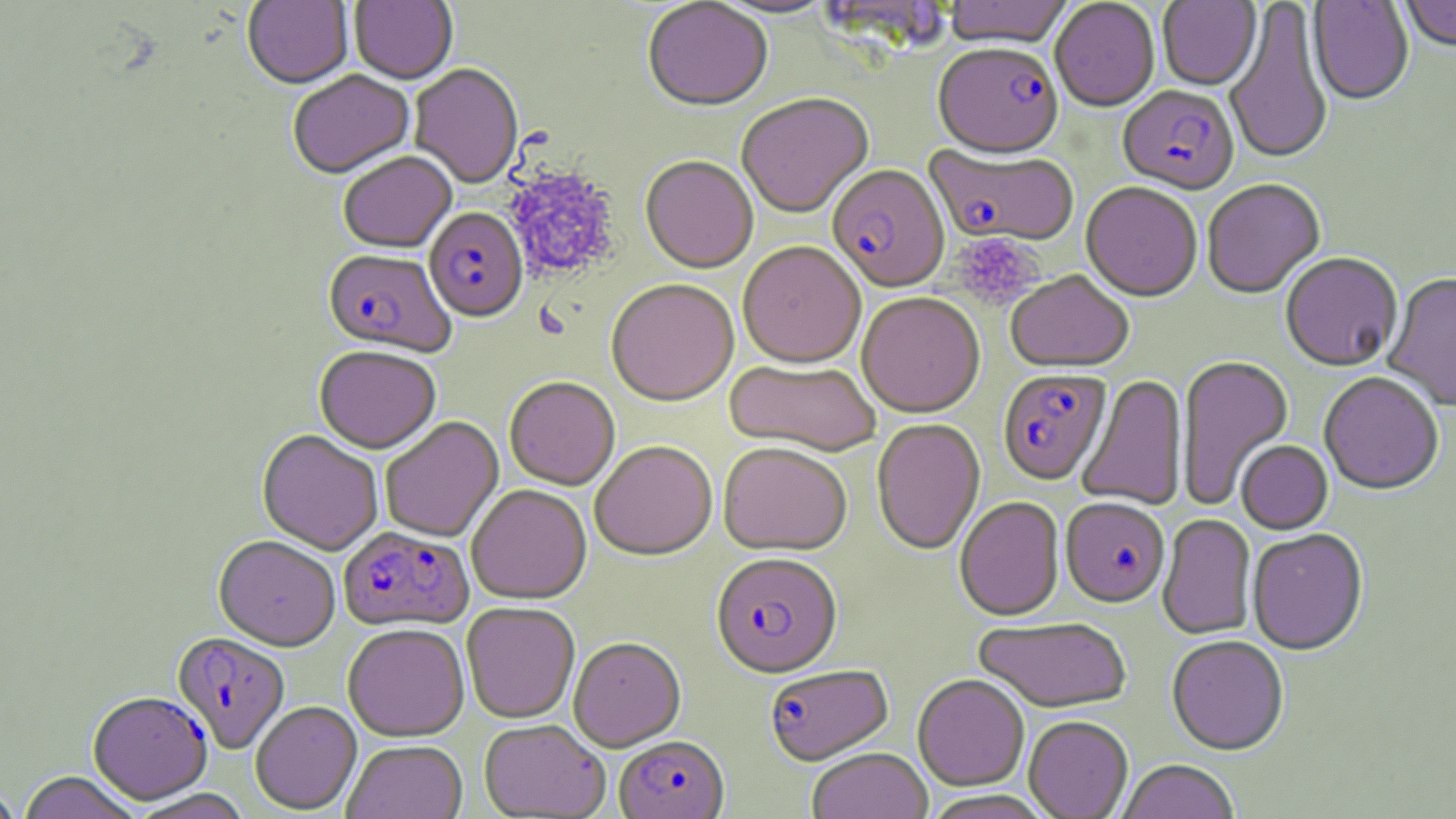 Approximate bounding boxes as [x1, y1, x2, y2] in pixels. Uninfected red blood cell locations: [242, 0, 353, 91], [349, 0, 458, 86], [943, 0, 1074, 52], [1224, 0, 1334, 169], [1401, 0, 1456, 54], [642, 1, 773, 115], [709, 1, 838, 21], [1050, 1, 1159, 114], [1157, 1, 1262, 92], [1307, 1, 1414, 107], [409, 65, 523, 189], [287, 72, 415, 181], [736, 95, 875, 220], [338, 154, 456, 255], [640, 157, 758, 276], [1202, 181, 1325, 300], [1080, 184, 1201, 304], [738, 243, 866, 372], [1281, 255, 1403, 374], [1006, 271, 1134, 375], [1383, 274, 1456, 412], [606, 281, 739, 410], [856, 293, 985, 420], [314, 347, 441, 455], [1176, 356, 1294, 510], [725, 361, 880, 459], [1077, 374, 1187, 512], [1319, 374, 1443, 498], [504, 379, 620, 491], [380, 417, 504, 543], [871, 420, 986, 556], [257, 431, 383, 556], [1236, 442, 1333, 535], [590, 443, 717, 562], [718, 445, 851, 559], [467, 486, 592, 605], [954, 497, 1065, 624], [1157, 515, 1257, 641], [1247, 531, 1369, 658], [213, 537, 340, 651], [461, 603, 580, 724], [973, 619, 1133, 714], [343, 625, 470, 742], [1166, 638, 1289, 758], [569, 639, 686, 753], [913, 676, 1029, 792], [250, 702, 363, 815], [1023, 717, 1133, 818], [479, 720, 610, 818], [342, 741, 467, 819], [807, 750, 933, 819], [1117, 761, 1240, 819], [17, 771, 143, 819], [0, 783, 23, 819], [127, 789, 253, 819], [921, 791, 1055, 819]. Plasmodium falciparum-infected red blood cell locations: [933, 45, 1064, 165], [1117, 87, 1239, 198], [924, 144, 1079, 248], [827, 166, 950, 296], [424, 209, 528, 325], [322, 251, 456, 359], [997, 370, 1111, 487], [1060, 500, 1171, 610], [338, 526, 474, 632], [711, 555, 843, 681], [171, 633, 290, 753], [764, 665, 894, 767], [88, 692, 213, 805], [614, 737, 729, 819]. Platelet locations: [503, 168, 619, 281], [951, 234, 1041, 312]. Slide-level diagnosis: Plasmodium falciparum. Light microscopy. Image is 1456×819 pixels. May-Grünwald-Giemsa stain. One field of a larger specimen. Thin blood film. 1000x magnification.